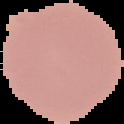

{
  "preparation": "thin blood film",
  "image_size": "124×124 pixels",
  "image_type": "cell region segmented out of the field of view; surrounding area masked to black",
  "malaria_status": "uninfected"
}